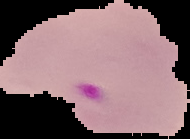

Summary:
  - Preparation: thin blood smear
  - Image size: 190×139 pixels
  - Malaria status: parasitized
  - Image type: segmented cell region with the area outside set to black